Classify this cell by malaria status.
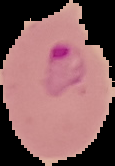

It is parasitized.

Summary:
  - Preparation: thin blood film
  - Image size: 115×166 pixels
  - Image type: segmented cell region with the area outside set to black